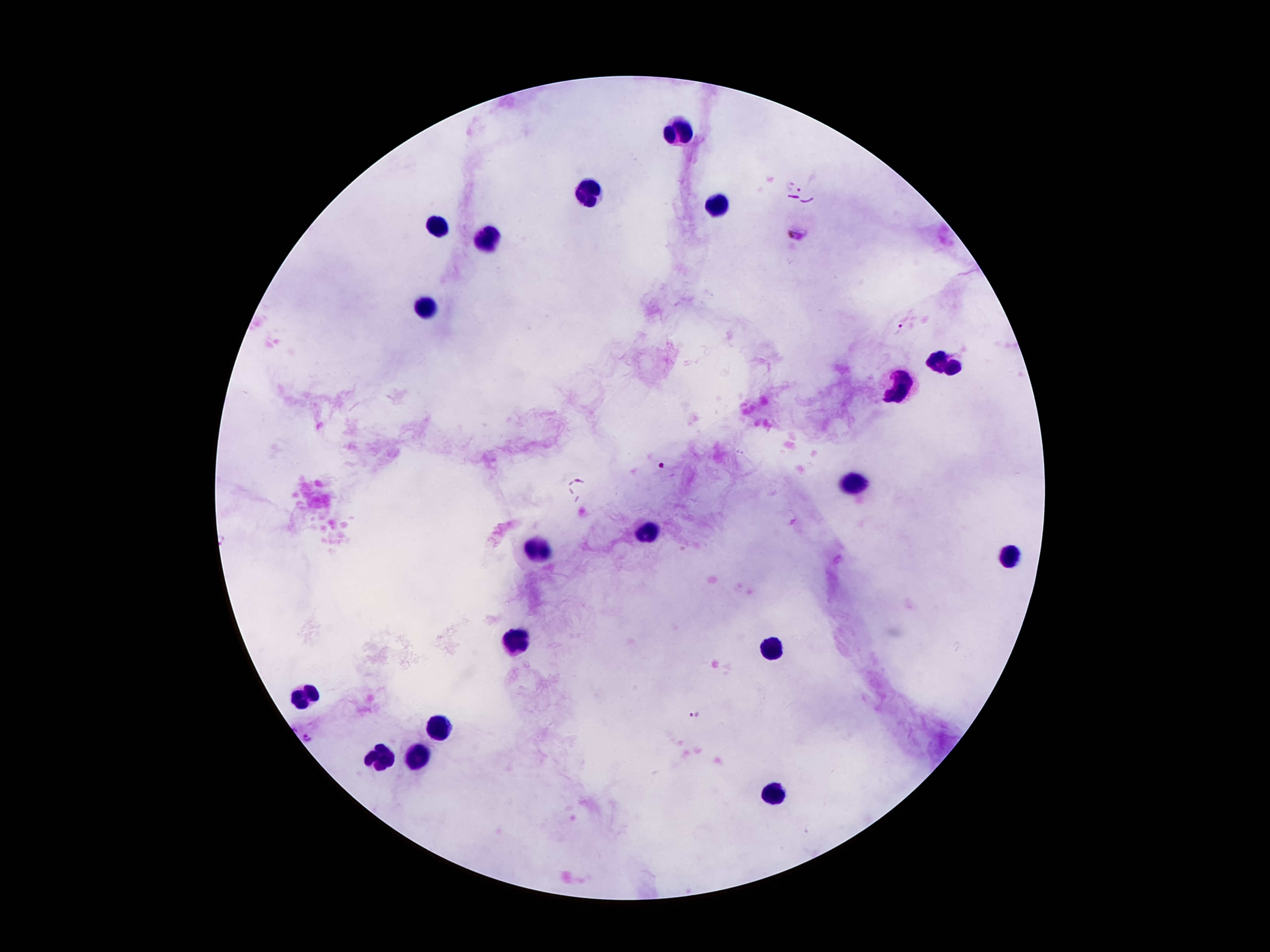
Approximate centers as (x, y) in pixels. Leukocyte locations: (678, 130), (590, 193), (709, 205), (436, 228), (492, 235), (424, 307), (942, 365), (898, 389), (853, 480), (648, 531), (538, 552), (1008, 557), (517, 638), (774, 645), (310, 694), (436, 725), (377, 757), (417, 757), (774, 792). Plasmodium parasite locations: (789, 184), (800, 189), (798, 234), (900, 329), (662, 467), (694, 714), (307, 739). Patient malaria status: positive for Plasmodium falciparum. Single field of view. Giemsa stain. Image is 1270×952 pixels. Thick blood film. Smartphone photograph taken through the microscope eyepiece. 100x magnification.